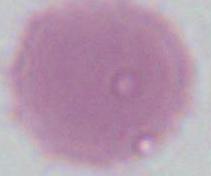 An erythrocyte is shown. Micrograph. 1000x magnification.